Assess the morphology of the red blood cells.
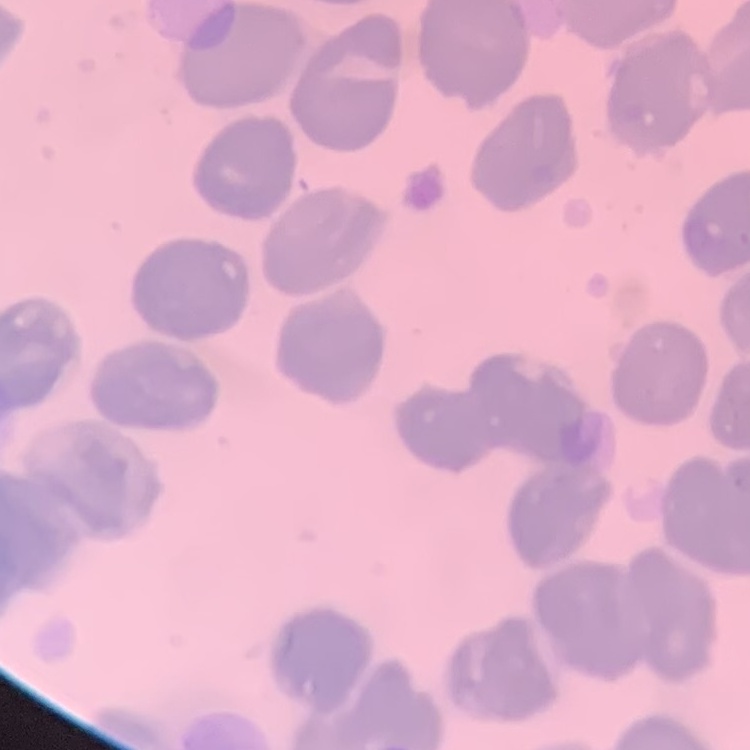

They show no rouleaux formation.

Summary:
  - Preparation: thin peripheral smear
  - Image type: square crop of a larger photomicrograph
  - Stain: Field's or Giemsa